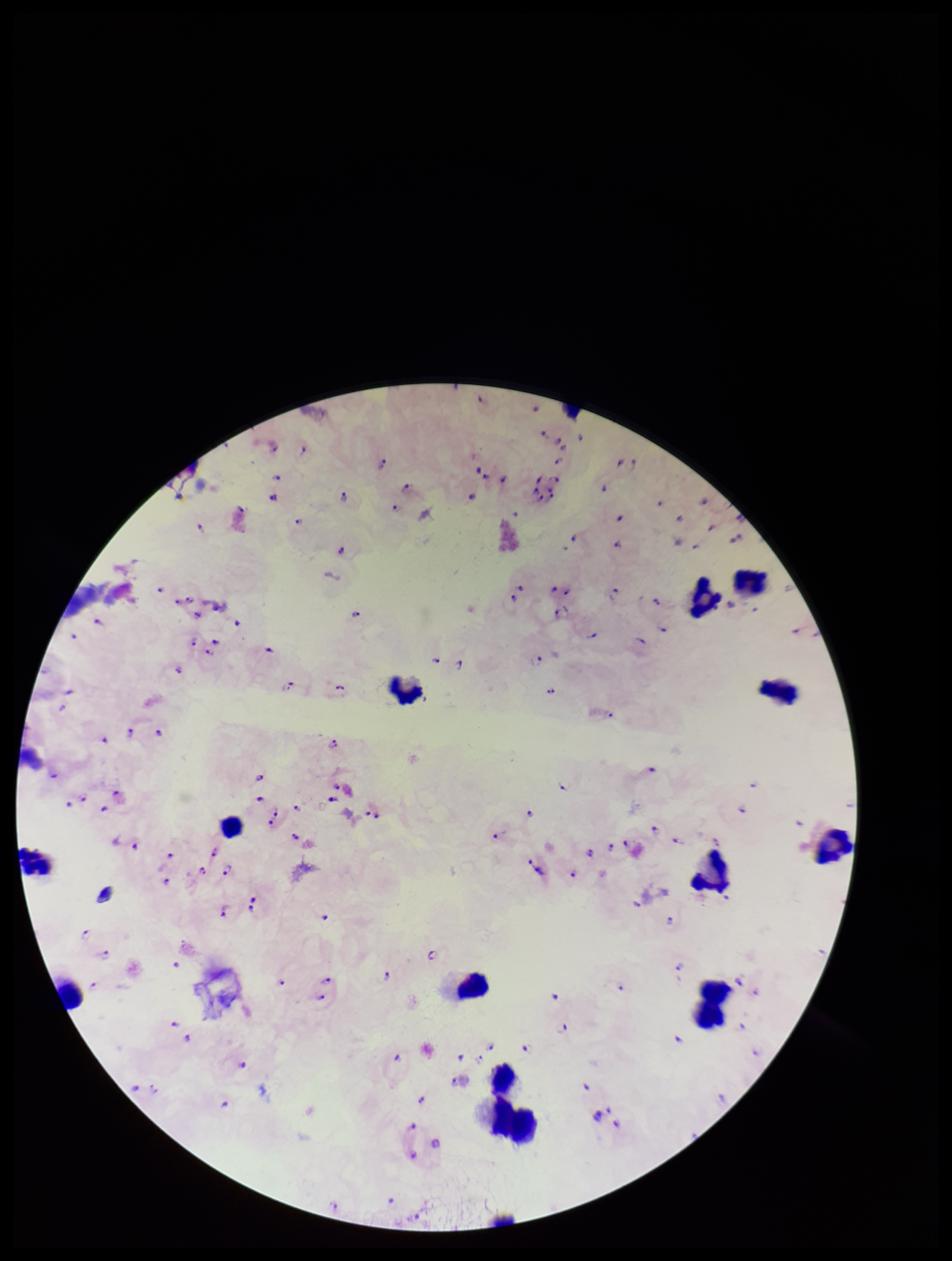

Giemsa stain. Image is 952×1261 pixels. Patient malaria status: infected. Parasite count: 106. Preparation: thick. Plasmodium parasites: detected. Leukocyte count: 13. One field from this slide. Smartphone photograph taken through the eyepiece of a microscope. Species reported for this patient: Plasmodium falciparum.